Report the malaria status of this cell.
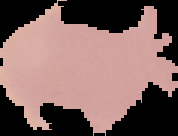
Uninfected.

image size = 178×136 pixels
preparation = thin blood film
image type = segmented cell region with the area outside set to black